Classify this cell by malaria status.
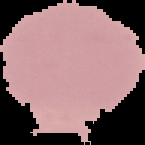

It is uninfected.

The area outside the segmented cell region is set to black. From a thin blood smear. Image is 145×145 pixels.